Give the position of every leukocyte visible.
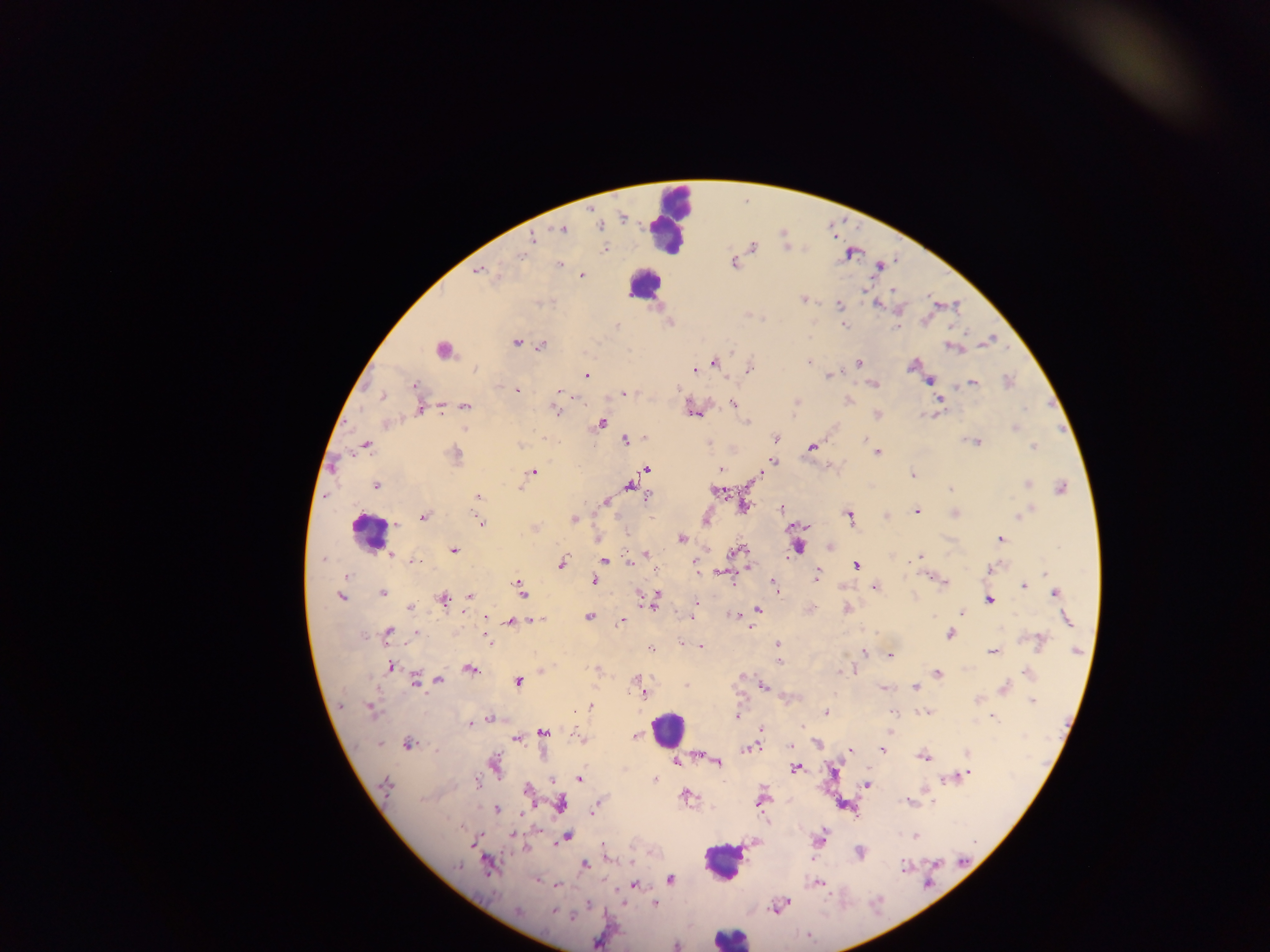
Approximate centers as (x, y) in pixels.
Leukocytes: (670, 216), (640, 283), (370, 531), (664, 730), (722, 864), (729, 937).

malaria_parasite_locations: 'approximate centers as (x, y) in pixels: (621, 218), (600, 226), (563, 229), (532, 241), (754, 248), (607, 250), (520, 258), (735, 264), (559, 265), (478, 272), (582, 275), (498, 276), (865, 289), (894, 291), (802, 299), (930, 303), (876, 305), (838, 306), (902, 309), (748, 314), (846, 326), (895, 329), (516, 344), (524, 344), (541, 346), (950, 346), (442, 351), (809, 361), (859, 361), (714, 362), (914, 365), (751, 367), (693, 370), (585, 375), (828, 376), (930, 382), (874, 383), (973, 383), (414, 384), (517, 390), (558, 392), (624, 392), (383, 396), (849, 401), (941, 401), (733, 402), (797, 403), (465, 406), (1024, 408), (418, 410), (441, 410), (555, 410), (692, 411), (697, 415), (876, 415), (601, 422), (748, 422), (385, 423), (464, 428), (1014, 428), (776, 436), (624, 440), (709, 441), (969, 441), (977, 441), (367, 445), (519, 445), (1032, 447), (813, 448), (875, 450), (351, 452), (877, 452), (772, 461), (335, 468), (646, 469), (533, 470), (717, 470), (912, 474), (1027, 483), (376, 486), (629, 487), (1061, 487), (520, 488), (949, 488), (715, 490), (479, 497), (647, 497), (605, 502), (747, 504), (743, 506), (780, 507), (916, 512), (848, 513), (957, 513), (885, 516), (1020, 516), (425, 517), (706, 519), (575, 520), (480, 522), (535, 528), (1002, 538), (680, 539), (799, 548), (742, 549), (454, 550), (736, 550), (646, 552), (390, 553), (923, 556), (917, 559), (411, 561), (606, 561), (696, 563), (563, 564), (630, 564), (855, 566), (750, 567), (989, 569), (818, 573), (1043, 573), (346, 575), (906, 577), (814, 579), (593, 581), (946, 583), (1023, 584), (775, 586), (875, 587), (522, 590), (776, 591), (656, 592), (383, 593), (1054, 593), (470, 596), (342, 598), (916, 598), (444, 599), (656, 599), (989, 599), (655, 605), (410, 607), (758, 609), (961, 610), (845, 611), (694, 612), (590, 615), (730, 615), (933, 616), (488, 617), (691, 617), (1066, 619), (533, 621), (622, 621), (511, 622), (751, 629), (389, 631), (874, 632), (417, 633), (486, 635), (949, 635), (1026, 637), (1039, 637), (487, 641), (681, 643), (702, 645), (777, 645), (649, 648), (1040, 648), (862, 652), (992, 653), (891, 656), (779, 662), (390, 666), (595, 669), (469, 670), (840, 671), (853, 671), (1029, 672), (939, 673), (636, 678), (416, 679), (438, 679), (518, 682), (685, 684), (1006, 684), (764, 686), (915, 687), (883, 688), (644, 695), (786, 699), (978, 700), (1033, 702), (591, 706), (341, 707), (368, 708), (371, 711), (828, 712), (893, 712), (926, 712), (737, 716), (490, 718), (994, 718), (469, 725), (800, 726), (760, 729), (577, 731), (544, 734), (636, 735), (511, 741), (380, 743), (408, 744), (817, 745), (747, 749), (882, 750), (849, 751), (967, 753), (923, 757), (677, 761), (718, 762), (795, 769), (971, 773), (966, 775), (654, 778), (947, 778), (578, 780), (384, 782), (867, 785), (478, 788), (923, 792), (686, 795), (761, 802), (561, 804), (533, 806), (930, 806), (595, 809), (495, 810), (524, 811), (591, 813), (512, 837), (568, 837), (914, 837), (563, 838), (753, 844), (741, 845), (470, 846), (740, 853), (628, 860), (584, 865), (460, 867), (902, 868), (486, 869), (670, 879), (812, 884), (818, 884), (559, 885), (632, 885), (622, 901), (654, 904), (590, 905), (775, 909), (518, 911), (551, 911)'
field_of_view: single
image_size: 1270×952 pixels
preparation: thick blood smear
capture: mobile-phone photograph through a microscope
country: Ghana